Outline each blood parasite and name the species.
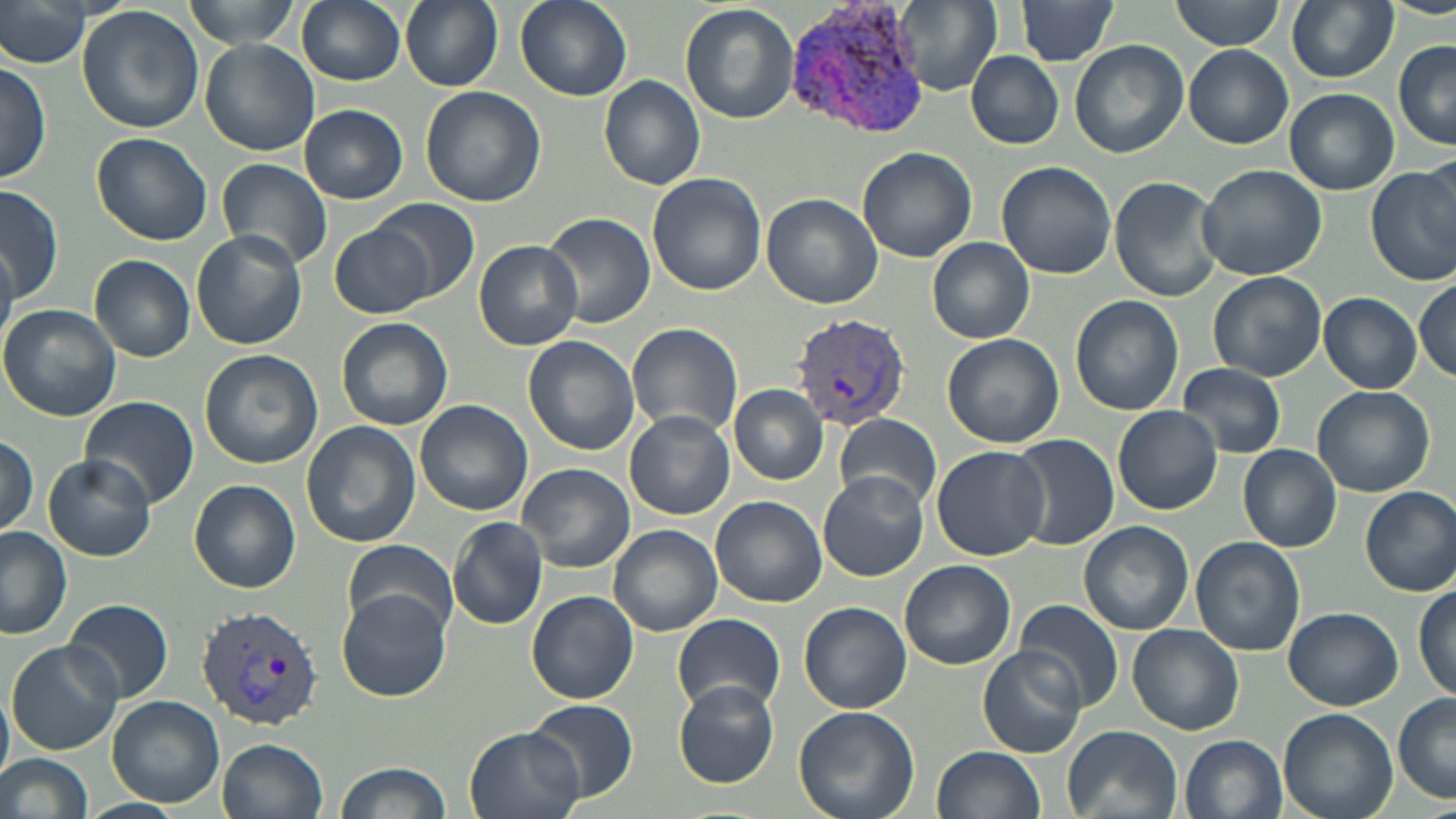

Approximate bounding boxes as named x1/y1/x2/y2 corners in pixels.
Plasmodium vivax-infected red blood cells: (x1=787, y1=2, x2=930, y2=139), (x1=792, y1=316, x2=913, y2=429), (x1=195, y1=605, x2=325, y2=730).
No Plasmodium falciparum, Plasmodium ovale, Plasmodium malariae, Babesia divergens, or Trypanosoma brucei observed.

Summary:
  - Uninfected red blood cell locations: (x1=0, y1=0, x2=91, y2=66), (x1=183, y1=0, x2=300, y2=51), (x1=296, y1=0, x2=407, y2=86), (x1=400, y1=0, x2=502, y2=90), (x1=515, y1=0, x2=632, y2=102), (x1=890, y1=0, x2=1004, y2=96), (x1=1012, y1=0, x2=1121, y2=64), (x1=1172, y1=0, x2=1285, y2=51), (x1=1286, y1=1, x2=1397, y2=83), (x1=679, y1=3, x2=799, y2=124), (x1=76, y1=5, x2=205, y2=134), (x1=1069, y1=39, x2=1189, y2=157), (x1=1394, y1=39, x2=1455, y2=149), (x1=201, y1=40, x2=320, y2=155), (x1=1185, y1=45, x2=1293, y2=147), (x1=967, y1=51, x2=1062, y2=148), (x1=0, y1=58, x2=51, y2=187), (x1=599, y1=75, x2=706, y2=189), (x1=420, y1=86, x2=545, y2=207), (x1=1285, y1=89, x2=1397, y2=196), (x1=299, y1=105, x2=407, y2=203), (x1=89, y1=133, x2=212, y2=246), (x1=857, y1=148, x2=978, y2=261), (x1=216, y1=157, x2=332, y2=271), (x1=995, y1=161, x2=1117, y2=279), (x1=1196, y1=163, x2=1326, y2=281), (x1=1366, y1=164, x2=1456, y2=287), (x1=646, y1=173, x2=767, y2=295), (x1=1109, y1=175, x2=1223, y2=302), (x1=0, y1=186, x2=63, y2=304), (x1=761, y1=193, x2=883, y2=309), (x1=372, y1=197, x2=478, y2=302), (x1=543, y1=211, x2=655, y2=328), (x1=330, y1=223, x2=435, y2=318), (x1=190, y1=229, x2=307, y2=350), (x1=927, y1=238, x2=1034, y2=344), (x1=0, y1=240, x2=18, y2=351), (x1=475, y1=240, x2=583, y2=349), (x1=90, y1=255, x2=195, y2=361), (x1=1208, y1=271, x2=1325, y2=382), (x1=1413, y1=277, x2=1455, y2=382), (x1=1320, y1=293, x2=1422, y2=393), (x1=1070, y1=295, x2=1185, y2=415), (x1=0, y1=305, x2=121, y2=423), (x1=336, y1=316, x2=453, y2=430), (x1=627, y1=322, x2=743, y2=438), (x1=942, y1=333, x2=1064, y2=449), (x1=524, y1=336, x2=640, y2=456), (x1=199, y1=348, x2=326, y2=470), (x1=1177, y1=364, x2=1286, y2=457), (x1=729, y1=384, x2=828, y2=484), (x1=1312, y1=386, x2=1435, y2=496), (x1=80, y1=397, x2=199, y2=507), (x1=415, y1=400, x2=532, y2=516), (x1=1113, y1=405, x2=1222, y2=513), (x1=625, y1=411, x2=734, y2=519), (x1=835, y1=413, x2=943, y2=511), (x1=301, y1=422, x2=420, y2=548), (x1=1009, y1=432, x2=1120, y2=550), (x1=0, y1=435, x2=39, y2=540), (x1=1238, y1=444, x2=1341, y2=551), (x1=931, y1=446, x2=1051, y2=561), (x1=42, y1=455, x2=157, y2=560), (x1=516, y1=463, x2=634, y2=572), (x1=817, y1=470, x2=930, y2=581), (x1=188, y1=479, x2=299, y2=593), (x1=1361, y1=488, x2=1455, y2=594), (x1=710, y1=495, x2=827, y2=608), (x1=447, y1=516, x2=548, y2=630), (x1=1079, y1=521, x2=1193, y2=635), (x1=611, y1=524, x2=721, y2=637), (x1=0, y1=527, x2=74, y2=640), (x1=1190, y1=536, x2=1305, y2=656), (x1=343, y1=539, x2=458, y2=635), (x1=900, y1=559, x2=1015, y2=669), (x1=1414, y1=582, x2=1455, y2=701), (x1=337, y1=590, x2=449, y2=701), (x1=527, y1=592, x2=638, y2=705), (x1=63, y1=598, x2=174, y2=704), (x1=1014, y1=600, x2=1123, y2=712), (x1=799, y1=602, x2=912, y2=714), (x1=1282, y1=606, x2=1401, y2=710), (x1=672, y1=613, x2=786, y2=714), (x1=1128, y1=623, x2=1244, y2=734), (x1=7, y1=641, x2=121, y2=756), (x1=976, y1=646, x2=1087, y2=758), (x1=674, y1=682, x2=780, y2=788), (x1=0, y1=689, x2=14, y2=782), (x1=1392, y1=693, x2=1455, y2=803), (x1=108, y1=695, x2=225, y2=806), (x1=522, y1=697, x2=640, y2=803), (x1=793, y1=704, x2=922, y2=819), (x1=1279, y1=708, x2=1397, y2=819), (x1=1062, y1=724, x2=1182, y2=819), (x1=464, y1=726, x2=585, y2=819), (x1=1181, y1=734, x2=1289, y2=819), (x1=218, y1=737, x2=329, y2=819), (x1=932, y1=745, x2=1045, y2=819), (x1=0, y1=753, x2=95, y2=819), (x1=330, y1=762, x2=451, y2=819), (x1=80, y1=798, x2=183, y2=819)
  - Slide-level diagnosis: Plasmodium vivax
  - Magnification: 1000x
  - Preparation: thin blood smear
  - Modality: optical microscopy
  - Image size: 1456×819 pixels
  - Field of view: single
  - Stain: May-Grünwald-Giemsa